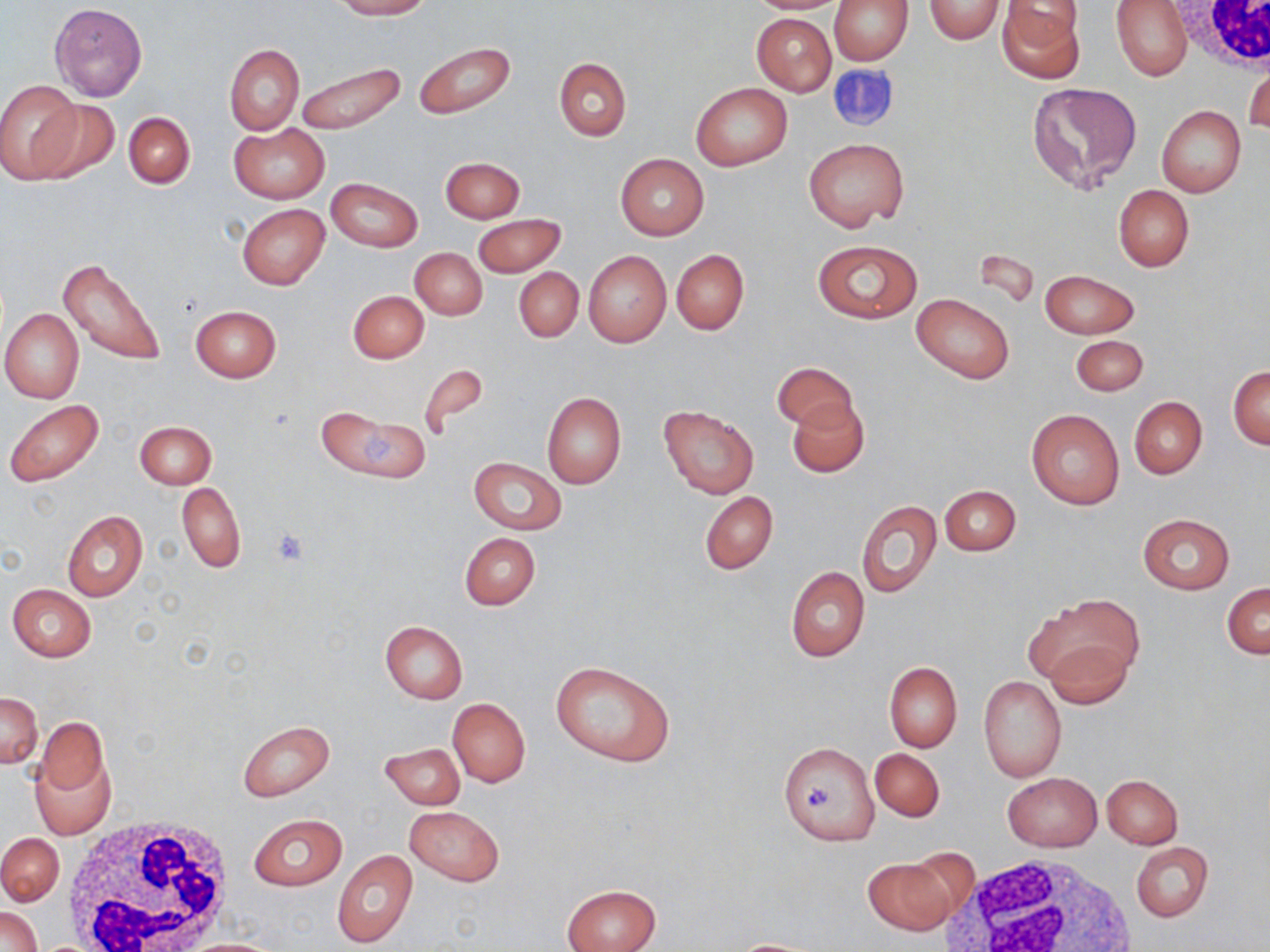 Approximate bounding boxes as named x1/y1/x2/y2 corners in pixels. Platelet locations: (x1=269, y1=526, x2=313, y2=568), (x1=800, y1=784, x2=839, y2=813). White blood cell locations: (x1=1165, y1=0, x2=1270, y2=73), (x1=61, y1=818, x2=239, y2=952), (x1=941, y1=851, x2=1143, y2=952). Uninfected red blood cell locations: (x1=332, y1=0, x2=429, y2=19), (x1=748, y1=0, x2=849, y2=14), (x1=830, y1=0, x2=913, y2=64), (x1=923, y1=0, x2=1004, y2=45), (x1=1112, y1=0, x2=1192, y2=80), (x1=996, y1=1, x2=1085, y2=80), (x1=49, y1=2, x2=148, y2=101), (x1=752, y1=13, x2=836, y2=95), (x1=413, y1=40, x2=516, y2=119), (x1=224, y1=44, x2=304, y2=135), (x1=554, y1=58, x2=631, y2=140), (x1=296, y1=61, x2=405, y2=136), (x1=1245, y1=61, x2=1269, y2=136), (x1=0, y1=80, x2=83, y2=182), (x1=1027, y1=82, x2=1142, y2=194), (x1=690, y1=83, x2=792, y2=170), (x1=29, y1=96, x2=119, y2=184), (x1=1156, y1=105, x2=1246, y2=197), (x1=124, y1=112, x2=195, y2=188), (x1=229, y1=122, x2=329, y2=204), (x1=804, y1=138, x2=908, y2=233), (x1=616, y1=154, x2=709, y2=240), (x1=440, y1=156, x2=524, y2=222), (x1=326, y1=177, x2=423, y2=252), (x1=1113, y1=184, x2=1194, y2=271), (x1=237, y1=204, x2=330, y2=290), (x1=472, y1=214, x2=564, y2=277), (x1=810, y1=239, x2=922, y2=324), (x1=411, y1=248, x2=487, y2=320), (x1=671, y1=249, x2=749, y2=334), (x1=583, y1=251, x2=671, y2=347), (x1=60, y1=258, x2=167, y2=366), (x1=515, y1=268, x2=583, y2=342), (x1=1040, y1=269, x2=1140, y2=338), (x1=348, y1=289, x2=429, y2=363), (x1=912, y1=293, x2=1015, y2=383), (x1=189, y1=305, x2=281, y2=382), (x1=0, y1=308, x2=84, y2=403), (x1=1071, y1=335, x2=1148, y2=396), (x1=418, y1=362, x2=491, y2=438), (x1=772, y1=362, x2=858, y2=433), (x1=1228, y1=366, x2=1269, y2=449), (x1=542, y1=392, x2=626, y2=488), (x1=1129, y1=396, x2=1207, y2=479), (x1=787, y1=399, x2=869, y2=477), (x1=6, y1=402, x2=104, y2=487), (x1=658, y1=403, x2=760, y2=499), (x1=314, y1=405, x2=426, y2=483), (x1=1027, y1=409, x2=1124, y2=509), (x1=135, y1=420, x2=216, y2=488), (x1=468, y1=457, x2=567, y2=534), (x1=177, y1=482, x2=246, y2=573), (x1=940, y1=484, x2=1020, y2=556), (x1=699, y1=491, x2=778, y2=575), (x1=856, y1=499, x2=940, y2=598), (x1=61, y1=510, x2=147, y2=602), (x1=1137, y1=513, x2=1234, y2=594), (x1=459, y1=532, x2=541, y2=610), (x1=785, y1=565, x2=869, y2=661), (x1=1222, y1=582, x2=1269, y2=659), (x1=7, y1=584, x2=95, y2=661), (x1=1038, y1=595, x2=1144, y2=686), (x1=379, y1=620, x2=467, y2=703), (x1=1044, y1=636, x2=1135, y2=709), (x1=549, y1=660, x2=675, y2=767), (x1=884, y1=661, x2=962, y2=752), (x1=979, y1=676, x2=1066, y2=782), (x1=0, y1=692, x2=42, y2=768), (x1=447, y1=697, x2=530, y2=787), (x1=35, y1=717, x2=110, y2=801), (x1=240, y1=720, x2=335, y2=801), (x1=379, y1=741, x2=465, y2=810), (x1=778, y1=741, x2=878, y2=845), (x1=869, y1=748, x2=944, y2=822), (x1=31, y1=749, x2=115, y2=839), (x1=1116, y1=773, x2=1196, y2=906), (x1=1002, y1=774, x2=1102, y2=852), (x1=1102, y1=774, x2=1183, y2=848), (x1=405, y1=805, x2=505, y2=886), (x1=247, y1=813, x2=347, y2=891), (x1=0, y1=832, x2=64, y2=905), (x1=1130, y1=841, x2=1213, y2=922), (x1=333, y1=848, x2=418, y2=948), (x1=861, y1=855, x2=963, y2=935), (x1=561, y1=883, x2=660, y2=952), (x1=0, y1=906, x2=42, y2=951), (x1=177, y1=938, x2=286, y2=952), (x1=727, y1=938, x2=829, y2=951). Slide-level diagnosis: no evidence of blood parasites. Captured at 1000x magnification. Thin blood film. Optical microscopy. Image is 1270×952 pixels. May-Grünwald-Giemsa-stained preparation. Single field of view.